Describe the morphology of the erythrocytes.
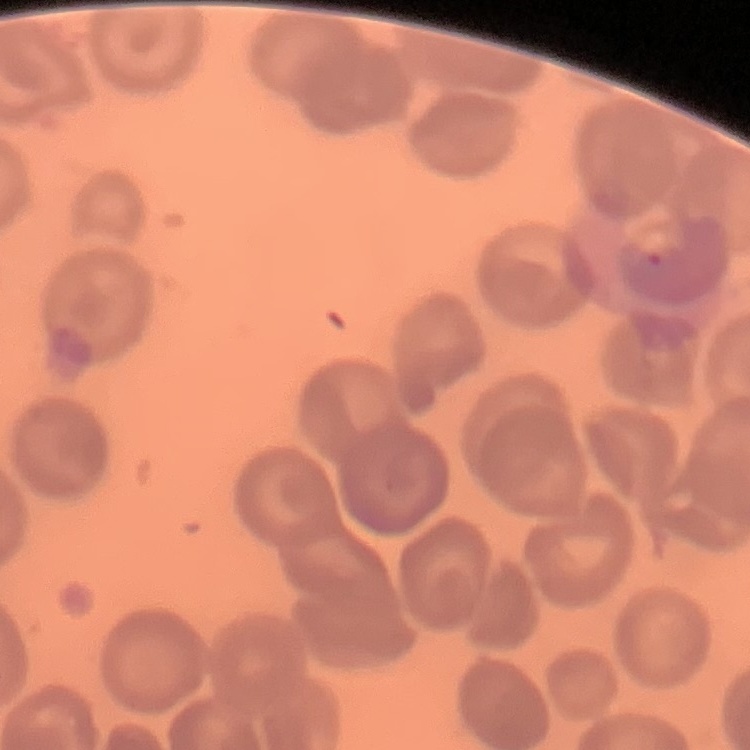

They show no rouleaux formation.

Summary:
  - Stain: Field's or Giemsa
  - Preparation: thin blood film
  - Image type: one tile cut from a larger photomicrograph